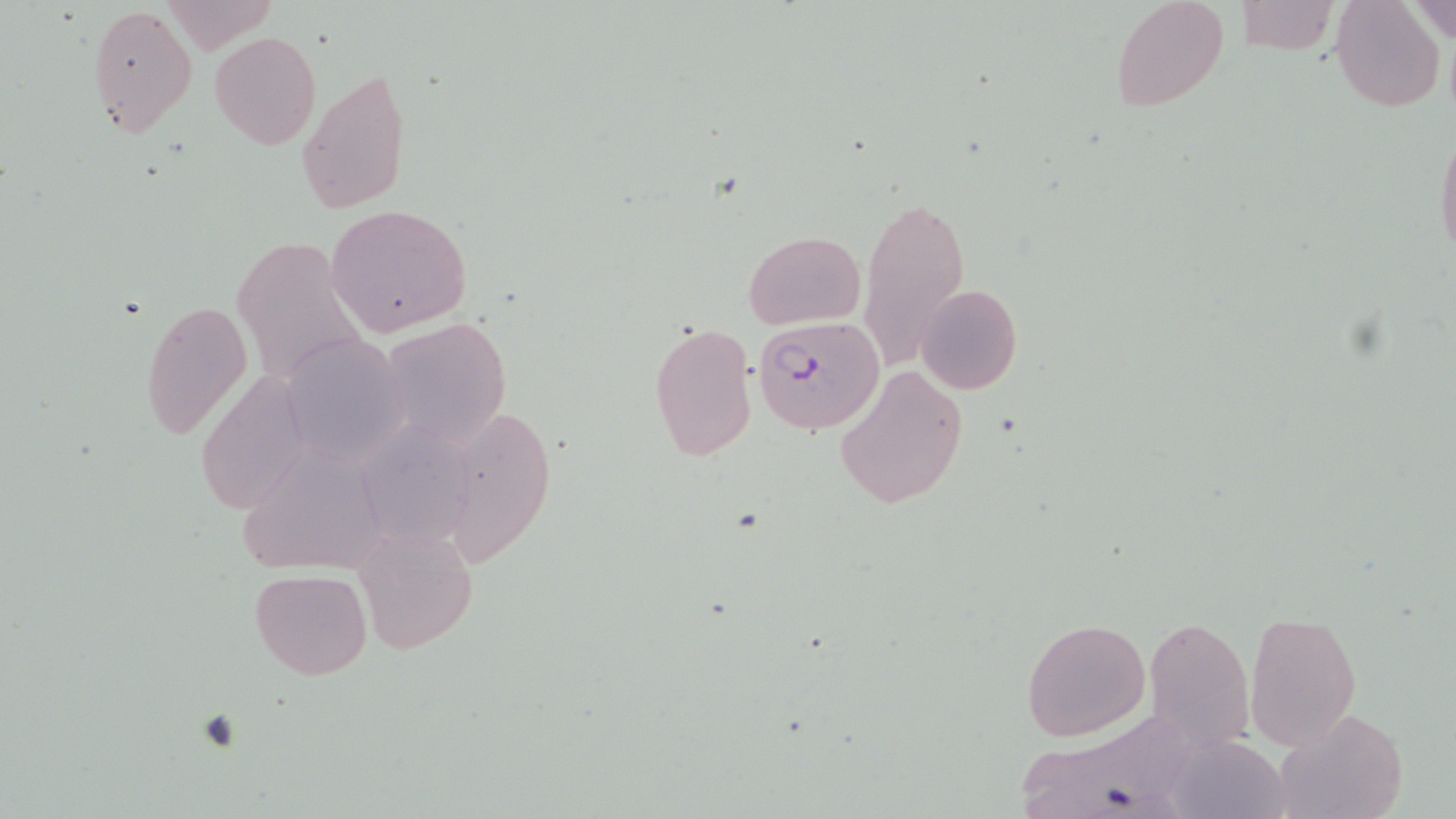 Approximate bounding boxes as (x1,y1)-(x2,y2) corner pairs in pixels. Uninfected red blood cell locations (subset): (1111,0)-(1230,113), (1331,0)-(1446,113), (1233,1)-(1338,54), (1403,1)-(1456,44), (86,3)-(197,140), (210,31)-(321,148), (298,67)-(412,216), (1433,125)-(1456,265), (856,191)-(970,372), (326,204)-(474,339), (744,230)-(866,329), (231,237)-(367,388), (916,283)-(1022,397), (139,297)-(250,442), (379,317)-(512,449), (647,320)-(757,462), (279,332)-(413,465), (833,365)-(970,511), (197,369)-(311,512), (436,403)-(558,572), (365,423)-(481,550), (244,449)-(406,587), (357,520)-(477,656), (249,569)-(373,679), (1245,610)-(1361,750), (1142,615)-(1256,750), (1020,616)-(1151,741), (1270,707)-(1408,819), (1018,712)-(1217,819), (1166,735)-(1289,819). Slide-level diagnosis: Plasmodium falciparum. Thin blood film. Captured at 1000x magnification. Optical microscopy. Image is 1456×819 pixels. May-Grünwald-Giemsa stain. One field of a larger specimen.